Outline platelets.
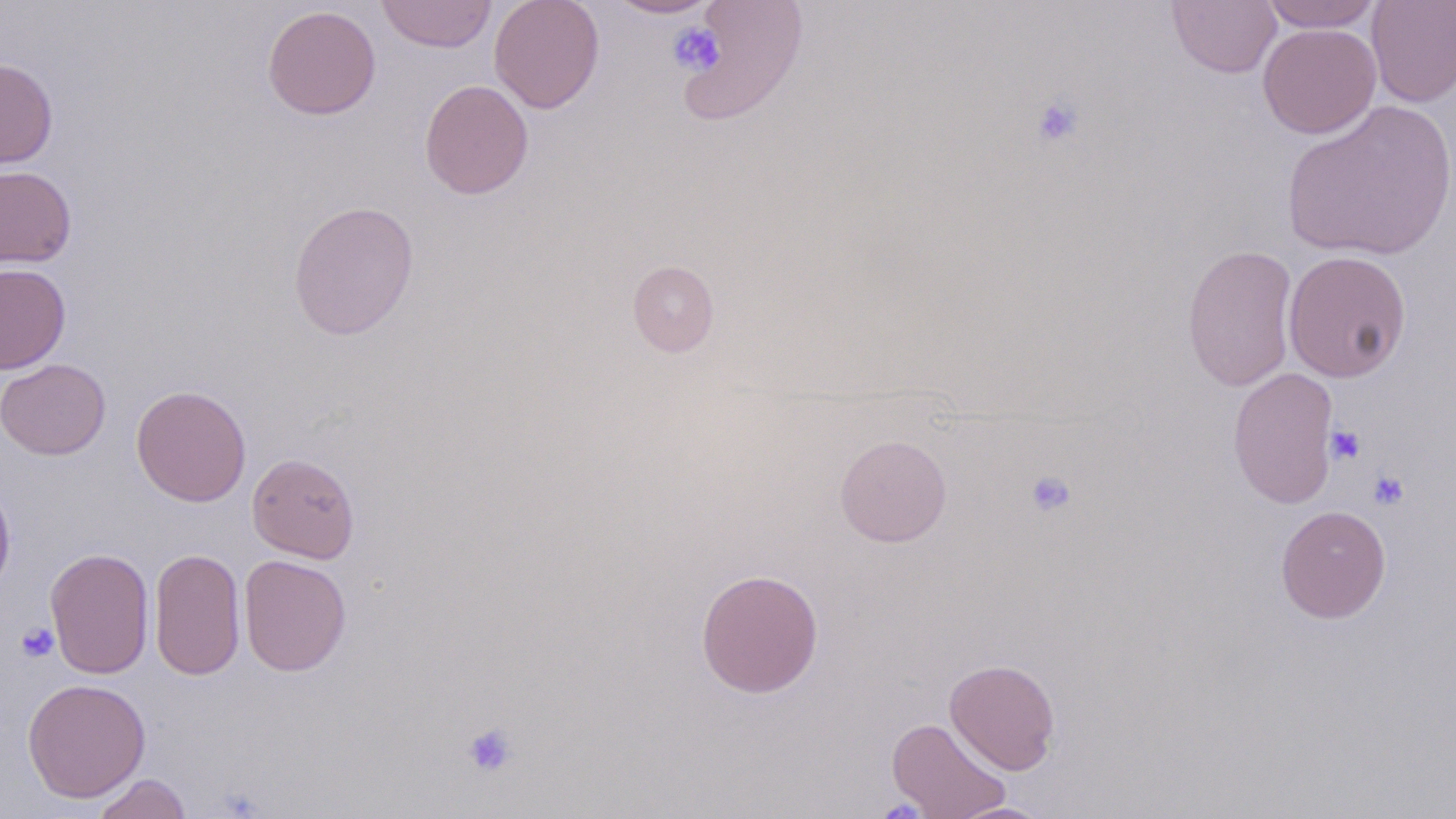

Approximate bounding boxes as (x1,y1)-(x2,y2) corner pairs in pixels.
Platelets: (668,22)-(725,76), (1030,95)-(1084,147), (1325,424)-(1365,465), (1024,469)-(1077,519), (1368,469)-(1410,511), (16,622)-(59,662), (462,721)-(519,779).

slide_level_diagnosis: negative for blood parasites
magnification: 1000x
preparation: thin blood film
image_size: 1456×819 pixels
field_of_view: single
modality: light microscopy
stain: May-Grünwald-Giemsa
uninfected_red_blood_cell_locations: 'approximate bounding boxes as (x1,y1)-(x2,y2) corner pairs in pixels: (375,0)-(497,53), (488,0)-(605,113), (605,0)-(720,19), (1167,0)-(1282,78), (1366,0)-(1456,107), (677,1)-(808,126), (1258,1)-(1383,32), (262,5)-(381,120), (1257,23)-(1381,139), (0,58)-(58,168), (419,79)-(533,199), (1281,99)-(1456,262), (0,165)-(76,268), (287,199)-(419,341), (1182,244)-(1299,392), (1283,250)-(1412,383), (628,260)-(719,357), (0,263)-(71,373), (0,358)-(110,460), (1227,366)-(1341,509), (131,385)-(251,507), (834,433)-(952,547), (247,453)-(360,564), (0,477)-(15,599), (1275,505)-(1391,623), (44,547)-(155,679), (149,547)-(245,681), (238,555)-(351,676), (695,568)-(824,698), (944,658)-(1061,775), (22,678)-(151,802), (886,717)-(1011,819), (91,773)-(192,819), (945,802)-(1055,819)'